Report the malaria status of this cell.
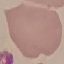

Uninfected.

Summary:
  - Stain: Giemsa
  - Image type: cell patch, automatically extracted from a larger field of view and resized to 64 × 64 pixels
  - Capture: smartphone through the microscope eyepiece
  - Preparation: thin smear